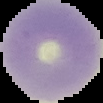

Summary:
  - Image type: cell region segmented out of the field of view; surrounding area masked to black
  - Image size: 103×103 pixels
  - Malaria status: uninfected
  - Preparation: thin blood film